Locate every Plasmodium falciparum-infected red blood cell.
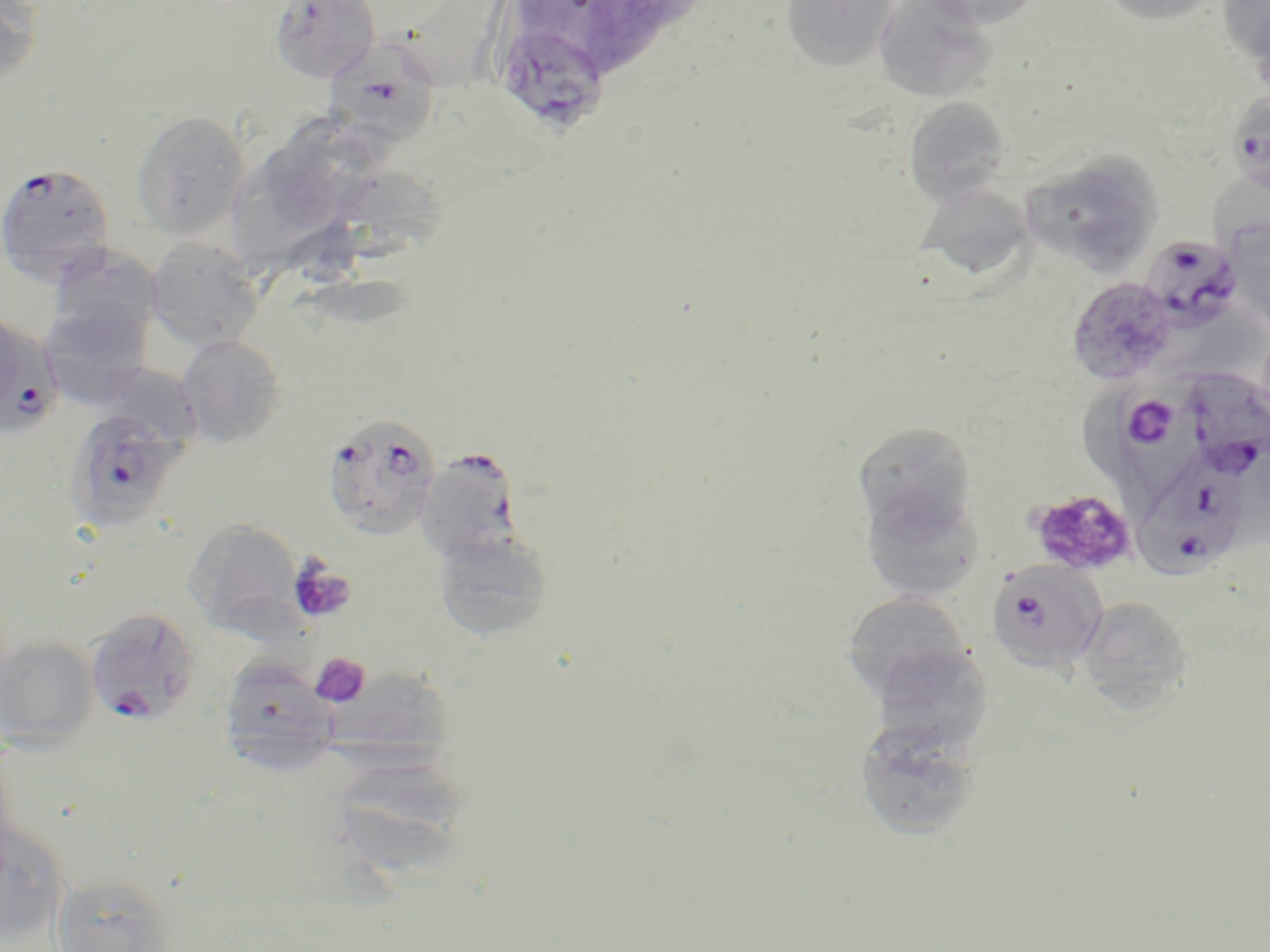

Approximate bounding boxes as (x1, y1, x2, y2) in pixels.
Plasmodium falciparum-infected red blood cells: (492, 22, 610, 136), (324, 44, 442, 150), (1225, 90, 1270, 195), (0, 163, 117, 286), (1138, 236, 1241, 330), (0, 309, 53, 434), (1186, 367, 1270, 478), (1119, 371, 1216, 484), (64, 406, 185, 535), (322, 413, 441, 539), (414, 447, 524, 564), (1138, 447, 1252, 578), (986, 560, 1108, 672), (84, 607, 201, 726).

slide-level diagnosis = Plasmodium falciparum
stain = May-Grünwald-Giemsa
image size = 1270×952 pixels
uninfected red blood cell locations = approximate bounding boxes as (x1, y1, x2, y2) in pixels: (272, 0, 384, 80), (387, 0, 528, 87), (590, 0, 666, 80), (779, 0, 899, 72), (921, 0, 1044, 29), (1096, 0, 1223, 26), (1219, 0, 1269, 77), (0, 1, 43, 89), (872, 1, 997, 103), (1247, 6, 1270, 104), (904, 96, 1011, 207), (131, 110, 249, 243), (260, 115, 372, 214), (1022, 154, 1164, 275), (233, 157, 340, 276), (322, 166, 454, 270), (913, 182, 1036, 282), (1222, 222, 1270, 332), (146, 237, 264, 352), (47, 249, 161, 356), (1066, 276, 1176, 384), (176, 335, 287, 448), (1080, 378, 1142, 490), (852, 421, 978, 537), (859, 481, 985, 604), (184, 519, 304, 635), (434, 530, 555, 641), (842, 591, 973, 704), (1076, 596, 1194, 715), (0, 637, 100, 750), (867, 645, 994, 754), (218, 657, 340, 772), (326, 667, 460, 780), (853, 716, 985, 843), (340, 759, 467, 873), (1, 819, 71, 944), (51, 873, 179, 952)
preparation = thin blood film
field of view = one of a larger specimen
modality = optical microscopy
platelet locations = approximate bounding boxes as (x1, y1, x2, y2) in pixels: (1027, 488, 1138, 576), (288, 559, 357, 625), (309, 653, 371, 708)
magnification = 1000x